Name the parasite shown.
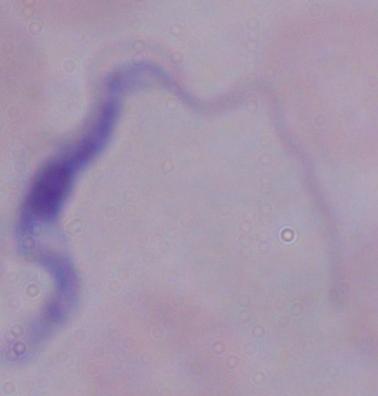

This is a trypanosome.

Summary:
  - Modality: photomicrograph
  - Magnification: 1000x